Outline each blood parasite and name the species.
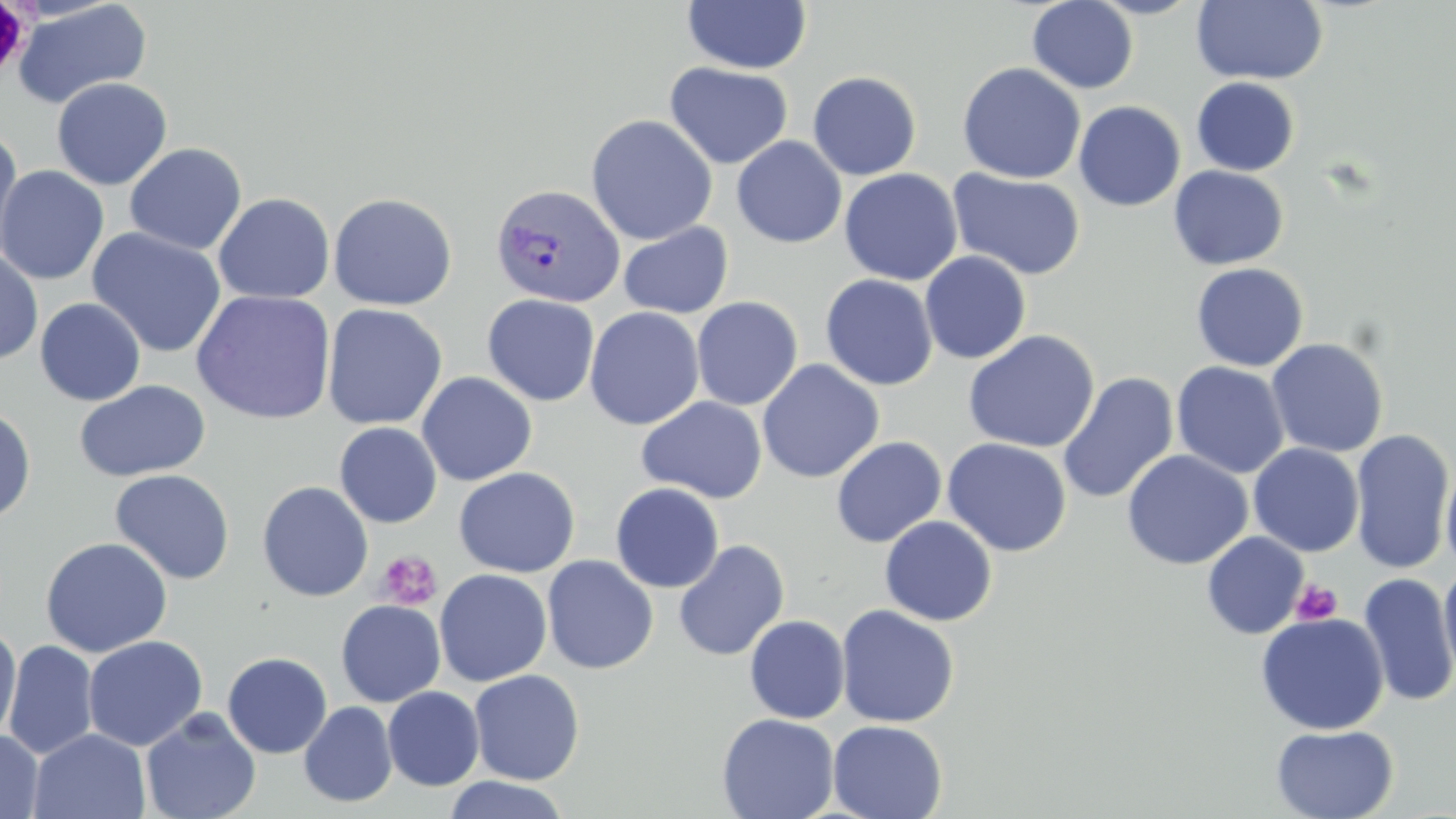

Approximate bounding boxes as (x1,y1)-(x2,y2) corner pairs in pixels.
Plasmodium vivax-infected red blood cells: (489,183)-(625,308).
No Plasmodium falciparum, Plasmodium ovale, Plasmodium malariae, Babesia divergens, or Trypanosoma brucei observed.

Summary:
  - Uninfected red blood cell locations: (1027,0)-(1139,93), (1087,0)-(1206,19), (12,1)-(152,110), (682,1)-(811,74), (1191,1)-(1329,85), (664,62)-(793,170), (957,62)-(1086,184), (807,71)-(921,180), (51,77)-(172,190), (1190,77)-(1300,177), (1074,100)-(1186,211), (585,114)-(719,245), (0,127)-(24,267), (732,136)-(847,248), (124,142)-(247,255), (0,165)-(109,285), (1168,166)-(1289,270), (839,168)-(962,286), (947,168)-(1086,281), (213,192)-(335,304), (328,192)-(458,311), (618,222)-(734,320), (87,227)-(227,358), (0,250)-(44,365), (920,251)-(1032,364), (1191,262)-(1309,372), (820,274)-(938,391), (191,290)-(336,424), (482,294)-(601,406), (691,296)-(803,410), (35,297)-(146,406), (321,303)-(447,431), (584,306)-(704,431), (963,330)-(1100,453), (1266,337)-(1389,458), (756,359)-(884,483), (1171,361)-(1290,479), (416,371)-(537,487), (1057,372)-(1179,505), (74,380)-(211,482), (636,396)-(768,504), (0,407)-(36,525), (334,422)-(442,528), (1349,429)-(1455,575), (830,436)-(947,547), (941,438)-(1072,557), (1248,443)-(1365,557), (1121,450)-(1253,570), (1440,458)-(1456,577), (453,467)-(580,578), (109,468)-(235,585), (257,481)-(373,602), (610,482)-(724,593), (880,515)-(998,626), (1202,532)-(1308,639), (40,536)-(173,657), (673,540)-(790,661), (541,555)-(658,674), (1439,561)-(1456,686), (434,568)-(552,686), (1358,572)-(1456,708), (335,599)-(446,707), (836,604)-(960,728), (1255,612)-(1390,735), (744,615)-(850,724), (0,622)-(22,745), (83,635)-(208,752), (4,640)-(99,760), (222,651)-(333,759), (468,669)-(585,785), (382,686)-(485,791), (299,701)-(398,807), (140,707)-(262,819), (717,713)-(839,819), (827,719)-(947,819), (1271,724)-(1399,818), (29,728)-(150,819), (0,729)-(44,819), (441,776)-(573,819)
  - Platelet locations: (1,2)-(34,83), (376,550)-(443,610), (1291,579)-(1343,625)
  - Slide-level diagnosis: Plasmodium vivax
  - Modality: optical microscopy
  - Stain: May-Grünwald-Giemsa
  - Image size: 1456×819 pixels
  - Magnification: 1000x
  - Field of view: one of a larger specimen
  - Preparation: thin blood smear